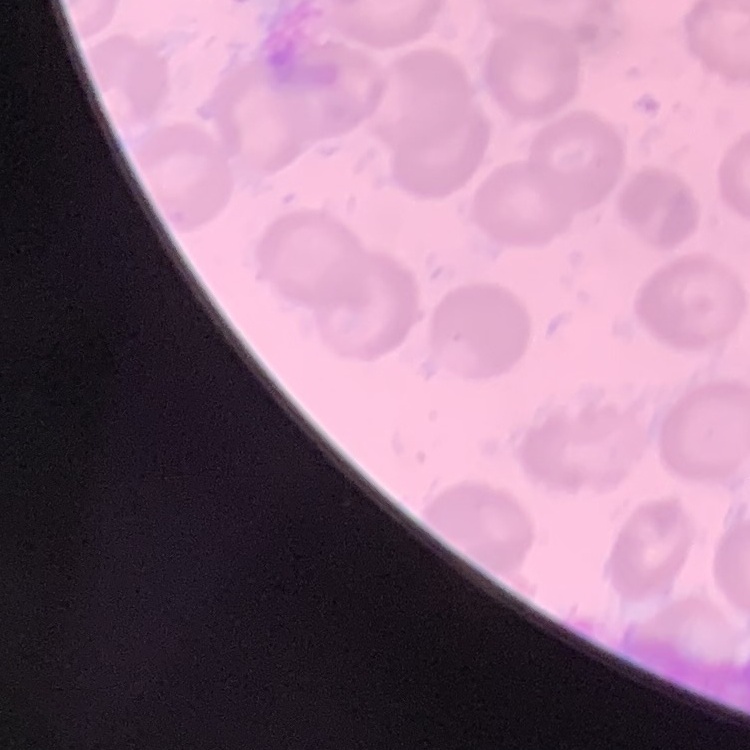 The erythrocytes show no rouleaux formation. One tile cut from a larger photomicrograph. Stained with either Field's or Giemsa. Thin blood film.